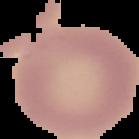
Summary:
  - Image type: segmented cell region on a black background
  - Image size: 139×139 pixels
  - Result: no Plasmodium parasites detected
  - Preparation: thin blood film